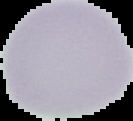
Image is 133×121 pixels. From a thin blood film. Malaria status: uninfected. Segmented cell region on a black background.